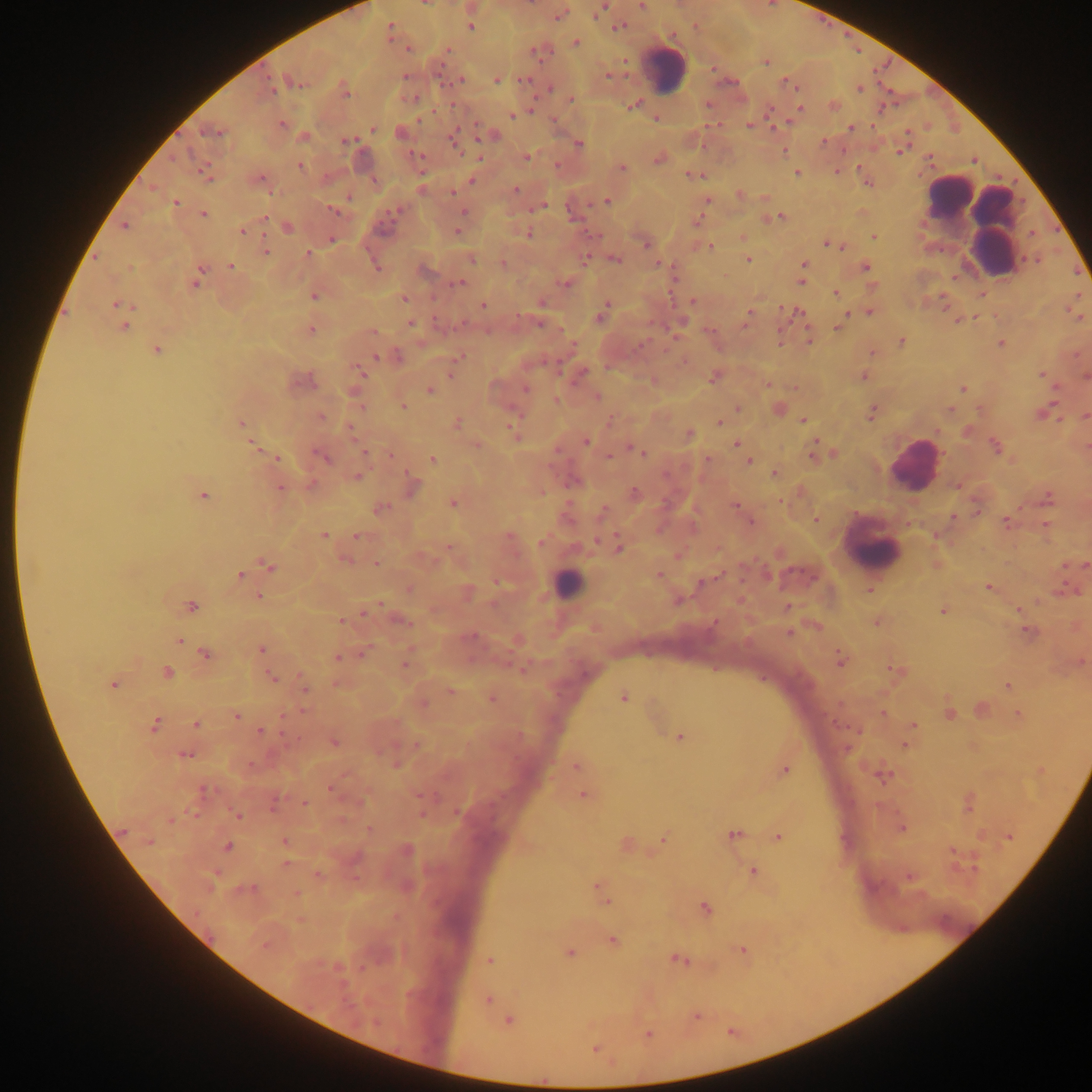

Approximate centers as [x, y] in pixels.
Summary:
  - Leukocyte locations: [667, 69], [948, 195], [986, 231], [911, 465], [873, 548], [568, 584]
  - Malaria parasite locations: [641, 5], [600, 9], [558, 16], [471, 27], [619, 27], [390, 28], [576, 42], [409, 48], [448, 50], [540, 52], [766, 62], [405, 76], [608, 76], [524, 79], [497, 81], [787, 82], [295, 83], [272, 88], [550, 88], [860, 89], [347, 93], [571, 99], [633, 105], [800, 109], [512, 115], [282, 124], [749, 124], [850, 128], [373, 129], [214, 132], [454, 138], [347, 141], [823, 142], [579, 143], [900, 151], [527, 157], [659, 158], [300, 166], [622, 169], [203, 171], [796, 173], [692, 175], [261, 179], [472, 180], [516, 191], [454, 192], [740, 195], [348, 198], [605, 201], [707, 201], [176, 203], [539, 207], [335, 211], [394, 211], [464, 213], [204, 214], [265, 217], [781, 217], [697, 222], [125, 226], [288, 227], [242, 231], [458, 232], [528, 234], [742, 237], [873, 237], [332, 239], [646, 244], [828, 245], [711, 246], [266, 250], [307, 253], [472, 259], [748, 259], [616, 260], [503, 264], [804, 265], [376, 266], [231, 267], [865, 267], [199, 272], [802, 281], [460, 283], [196, 284], [565, 284], [836, 293], [314, 296], [403, 299], [693, 301], [542, 303], [116, 304], [483, 305], [870, 313], [748, 315], [600, 317], [844, 318], [957, 321], [411, 323], [124, 327], [838, 327], [311, 330], [809, 340], [901, 342], [1001, 343], [157, 350], [872, 352], [376, 356], [460, 357], [582, 372], [361, 373], [1042, 374], [451, 375], [863, 376], [1086, 376], [713, 379], [525, 388], [963, 389], [430, 390], [596, 396], [556, 401], [403, 407], [739, 408], [950, 409], [872, 413], [1086, 416], [321, 417], [803, 420], [610, 421], [719, 422], [240, 423], [456, 424], [513, 430], [689, 434], [586, 442], [736, 444], [477, 445], [252, 446], [996, 447], [637, 451], [364, 452], [391, 455], [812, 455], [322, 457], [608, 457], [276, 458], [708, 458], [432, 459], [749, 461], [775, 472], [358, 477], [311, 484], [280, 488], [634, 493], [203, 496], [453, 504], [734, 505], [380, 509], [601, 512], [953, 517], [816, 519], [1005, 521], [750, 522], [1046, 525], [324, 535], [357, 536], [597, 541], [541, 543], [449, 547], [619, 547], [345, 560], [376, 563], [270, 566], [1085, 566], [659, 574], [240, 575], [496, 581], [701, 582], [988, 587], [409, 589], [869, 590], [258, 596], [381, 605], [192, 606], [787, 607], [943, 611], [364, 614], [402, 621], [341, 622], [1028, 632], [788, 633], [180, 641], [261, 649], [206, 655], [362, 655], [337, 657], [840, 659], [405, 663], [895, 669], [167, 672], [272, 678], [114, 684], [1008, 685], [304, 687], [451, 691], [623, 697], [491, 698], [425, 703], [884, 712], [950, 714], [1018, 714], [283, 715], [236, 716], [196, 724], [913, 725], [155, 726], [260, 731], [680, 738], [334, 743], [416, 745], [906, 745], [186, 755], [576, 766], [785, 771], [883, 775], [331, 789], [582, 795], [305, 803], [237, 815], [422, 815], [369, 829], [902, 829], [123, 830], [734, 834], [779, 837], [1009, 837], [663, 839], [149, 842], [285, 842], [228, 846], [286, 864], [754, 871], [317, 874], [598, 887], [295, 894], [606, 902], [706, 909], [613, 941], [265, 946], [741, 950], [569, 953], [489, 960], [678, 960], [488, 1000], [697, 1017], [508, 1021], [648, 1034], [595, 1049]
  - Capture: mobile-phone photograph through a microscope
  - Preparation: thick blood film
  - Country: Ghana
  - Field of view: single
  - Image size: 1092×1092 pixels